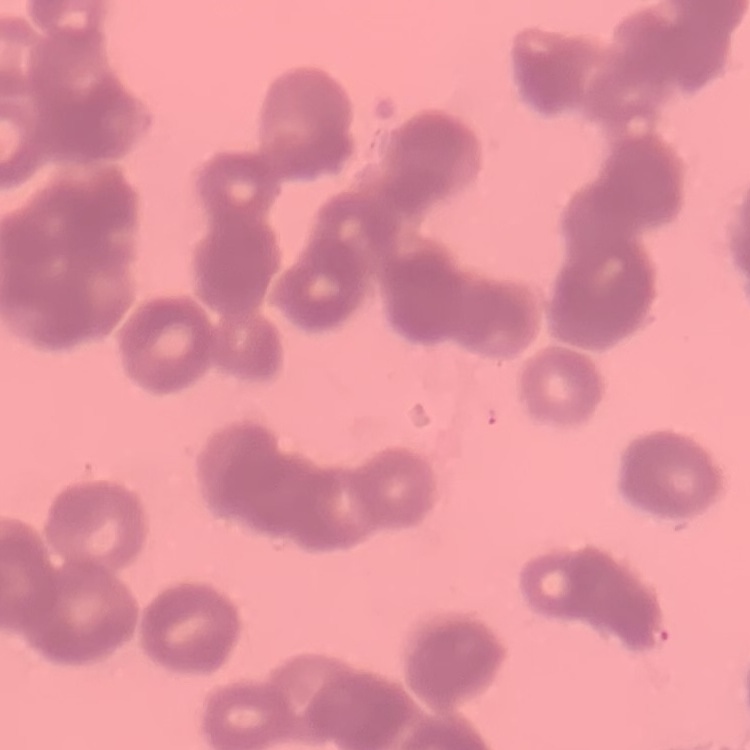
erythrocyte morphology = rouleaux formation
preparation = thin blood film
image type = square crop of a larger photomicrograph
stain = Field's or Giemsa